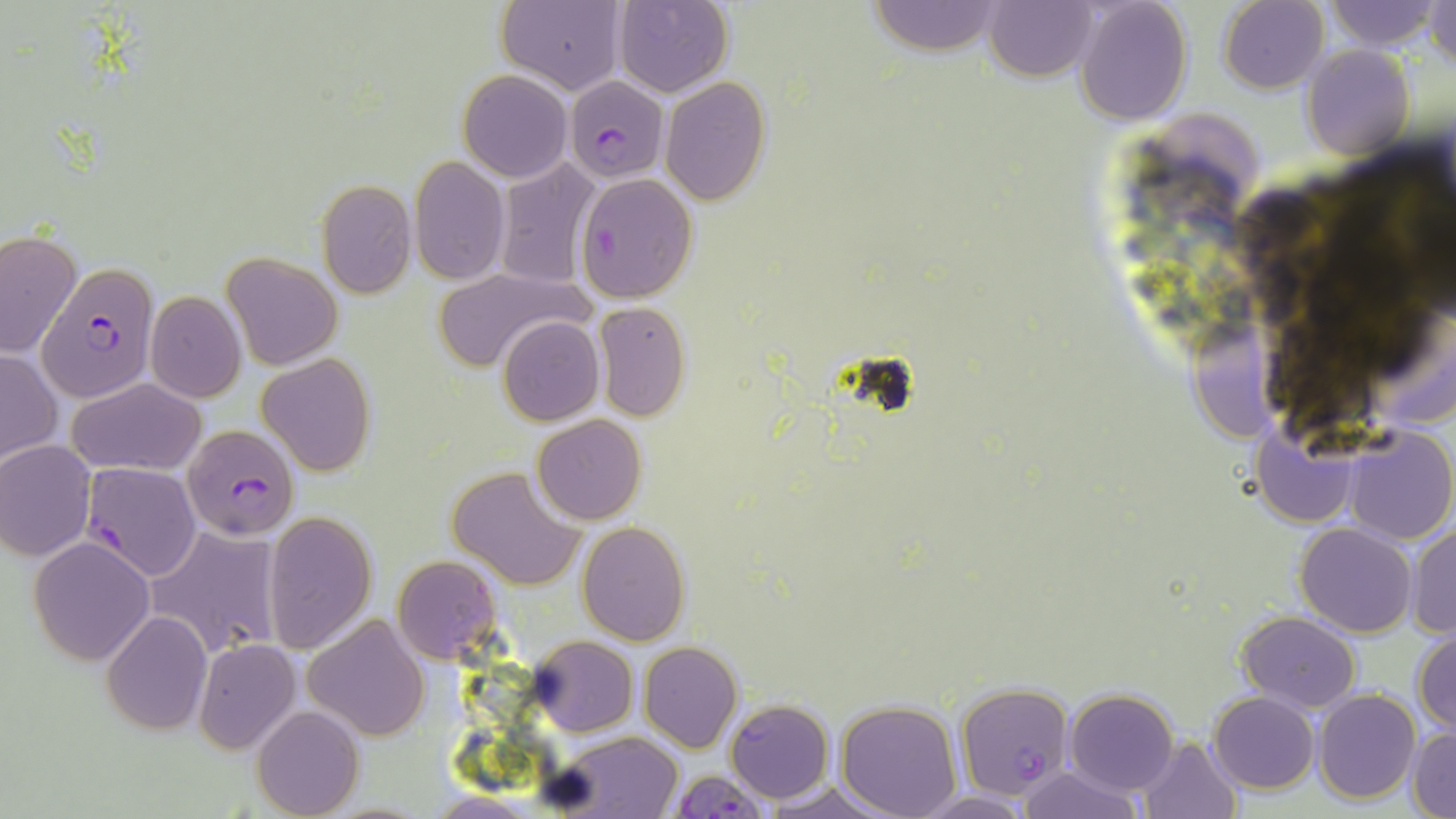

slide-level diagnosis = Plasmodium falciparum
modality = light microscopy
image size = 1456×819 pixels
magnification = 1000x
stain = May-Grünwald-Giemsa
preparation = thin blood film
uninfected red blood cell locations = approximate bounding boxes as [x1, y1, x2, y2] in pixels: [496, 0, 625, 94], [614, 0, 733, 97], [985, 0, 1097, 82], [1218, 0, 1329, 92], [1325, 0, 1441, 50], [1427, 0, 1456, 70], [864, 1, 1006, 54], [1075, 1, 1192, 123], [1300, 44, 1414, 159], [458, 70, 571, 183], [661, 77, 772, 205], [434, 105, 549, 249], [409, 156, 510, 285], [491, 157, 604, 289], [576, 172, 700, 303], [316, 179, 417, 298], [0, 230, 81, 359], [221, 252, 342, 370], [432, 267, 589, 372], [144, 290, 247, 403], [591, 300, 691, 420], [1187, 309, 1287, 445], [497, 315, 604, 425], [0, 349, 61, 466], [257, 354, 376, 475], [65, 376, 205, 477], [532, 414, 646, 524], [1251, 415, 1361, 529], [1342, 425, 1456, 544], [0, 439, 95, 561], [1323, 451, 1450, 619], [448, 465, 586, 590], [263, 510, 378, 653], [576, 521, 690, 646], [1295, 522, 1417, 637], [147, 523, 281, 658], [1406, 526, 1456, 637], [29, 535, 156, 666], [391, 554, 501, 664], [1236, 610, 1360, 712], [102, 611, 212, 735], [302, 614, 431, 742], [1412, 625, 1456, 735], [530, 635, 638, 736], [193, 638, 302, 756], [639, 642, 743, 752], [1065, 687, 1179, 795], [1313, 690, 1420, 805], [1210, 691, 1319, 794], [834, 699, 962, 818], [251, 705, 364, 818], [1408, 728, 1455, 819], [546, 733, 684, 817], [1136, 736, 1243, 818], [1018, 765, 1143, 819], [764, 780, 899, 819], [911, 790, 1035, 817], [428, 792, 539, 818]
Plasmodium falciparum-infected red blood cell locations = approximate bounding boxes as [x1, y1, x2, y2] in pixels: [564, 76, 669, 181], [36, 265, 161, 401], [183, 423, 303, 541], [80, 463, 203, 581], [955, 683, 1073, 798], [725, 700, 833, 803], [666, 769, 770, 818]
field of view = one of a larger specimen